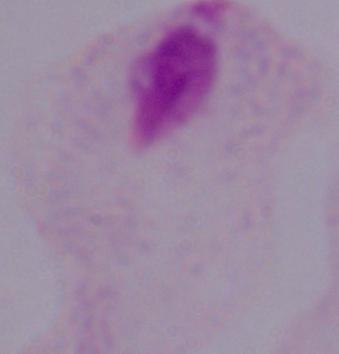
modality = photomicrograph
identification = trichomonad
magnification = 1000x